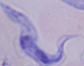
Photomicrograph. A trypanosome is seen. 1000x magnification.